Report the malaria status of this cell.
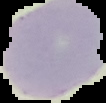

Uninfected.

image type = segmented cell region on a black background
image size = 106×103 pixels
preparation = thin blood smear